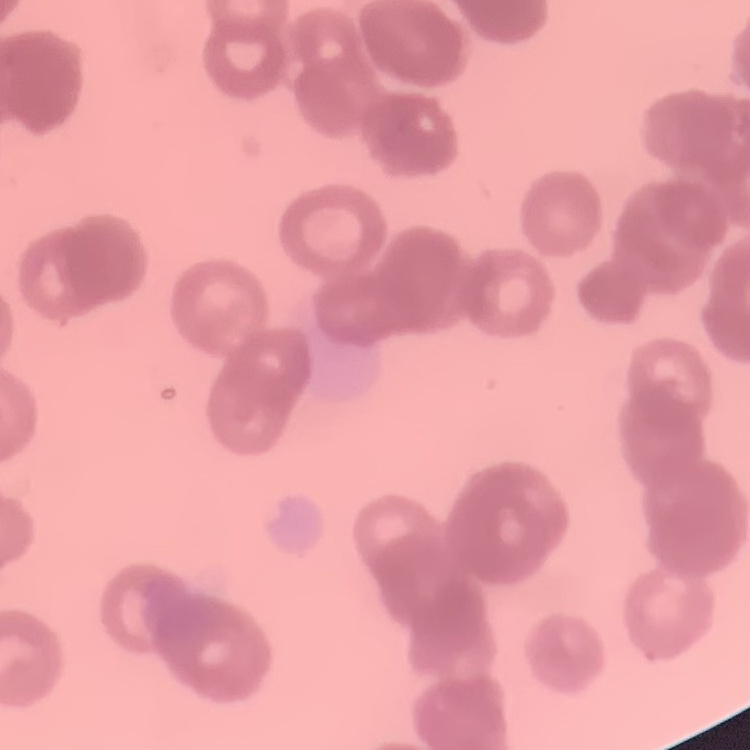

Summary:
  - Erythrocyte morphology: rouleaux formation
  - Preparation: thin peripheral smear
  - Image type: square crop of a larger photomicrograph
  - Stain: Field's or Giemsa